Report the malaria status of this cell.
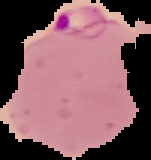

It is parasitized.

Image is 151×160 pixels. From a thin blood smear. Cell region segmented out of the field of view; the surrounding area is masked to black.